Assess for malaria.
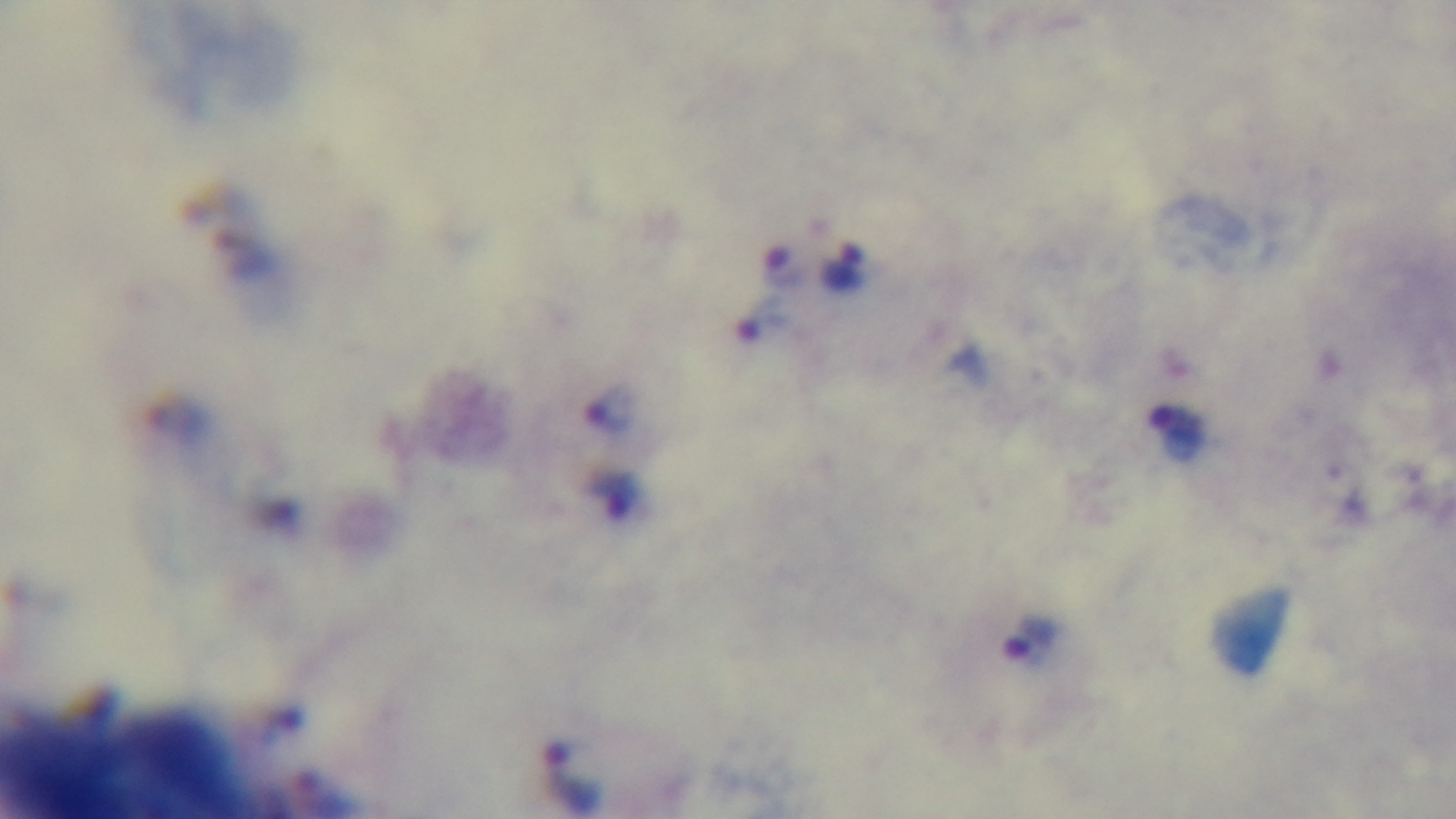
Positive.

Summary:
  - Stain: Giemsa
  - Modality: light microscopy
  - Objective: 100x oil immersion
  - Field of view: one from the slide
  - Preparation: thick
  - Capture: mounted 4K digital camera